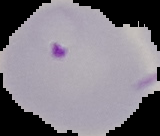

Summary:
  - Image size: 160×136 pixels
  - Malaria status: parasitized
  - Preparation: thin blood film
  - Image type: segmented cell region on a black background